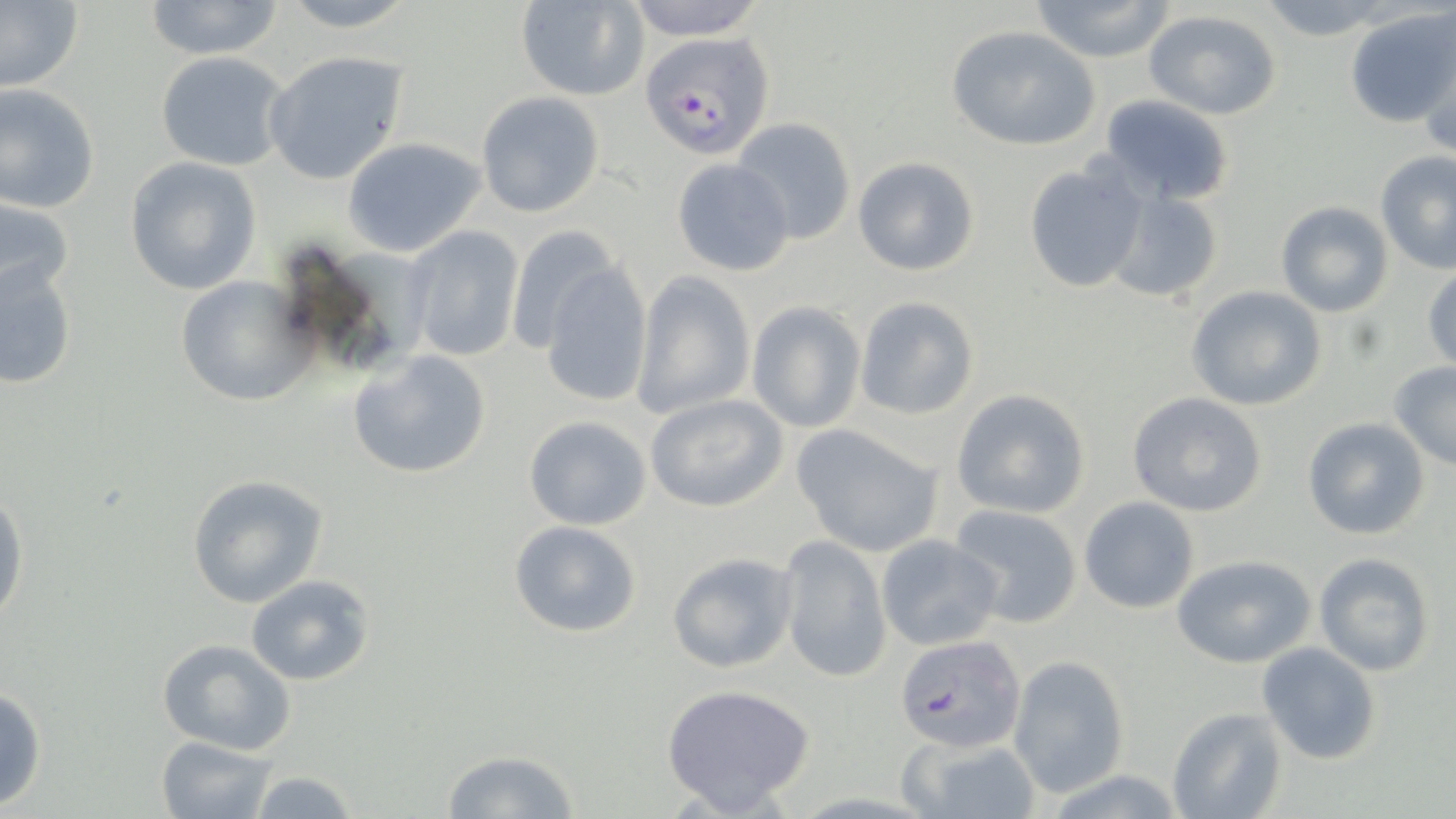
slide-level diagnosis = Plasmodium falciparum
magnification = 1000x
field of view = single
stain = May-Grünwald-Giemsa
image size = 1456×819 pixels
uninfected red blood cell locations = approximate bounding boxes as [x1, y1, x2, y2] in pixels: [0, 0, 84, 93], [141, 0, 287, 60], [272, 0, 424, 32], [514, 0, 648, 101], [618, 0, 771, 40], [1029, 0, 1175, 64], [1255, 0, 1394, 39], [1348, 8, 1455, 127], [1142, 11, 1285, 120], [946, 26, 1101, 150], [261, 50, 410, 186], [154, 52, 294, 172], [0, 84, 101, 214], [475, 91, 604, 218], [1100, 94, 1234, 205], [729, 116, 856, 246], [341, 137, 487, 258], [1375, 151, 1456, 274], [123, 156, 263, 296], [852, 157, 979, 276], [670, 158, 794, 277], [1023, 160, 1147, 294], [1103, 189, 1224, 306], [0, 192, 76, 307], [1275, 201, 1393, 317], [402, 224, 526, 362], [505, 226, 620, 354], [2, 256, 78, 388], [539, 262, 655, 409], [1423, 263, 1455, 374], [630, 270, 756, 421], [174, 274, 319, 408], [1187, 286, 1327, 410], [855, 296, 978, 420], [746, 302, 867, 433], [348, 348, 494, 481], [1388, 361, 1456, 470], [951, 389, 1090, 518], [1127, 391, 1269, 517], [645, 393, 789, 513], [521, 414, 655, 530], [1301, 417, 1431, 540], [791, 423, 944, 557], [186, 473, 329, 608], [0, 487, 29, 630], [1079, 496, 1199, 613], [947, 502, 1084, 628], [508, 521, 643, 638], [777, 534, 892, 684], [876, 534, 1003, 652], [666, 550, 798, 674], [1312, 553, 1436, 677], [1172, 554, 1320, 670], [245, 574, 376, 686], [156, 637, 297, 755], [1256, 641, 1383, 766], [1009, 655, 1132, 799], [660, 683, 817, 814], [0, 686, 49, 813], [1165, 705, 1288, 819], [898, 734, 1041, 818], [155, 735, 278, 818], [440, 750, 582, 819], [246, 768, 360, 819]
preparation = thin blood smear
Plasmodium falciparum-infected red blood cell locations = approximate bounding boxes as [x1, y1, x2, y2] in pixels: [641, 33, 775, 157], [895, 633, 1028, 753]
modality = light microscopy